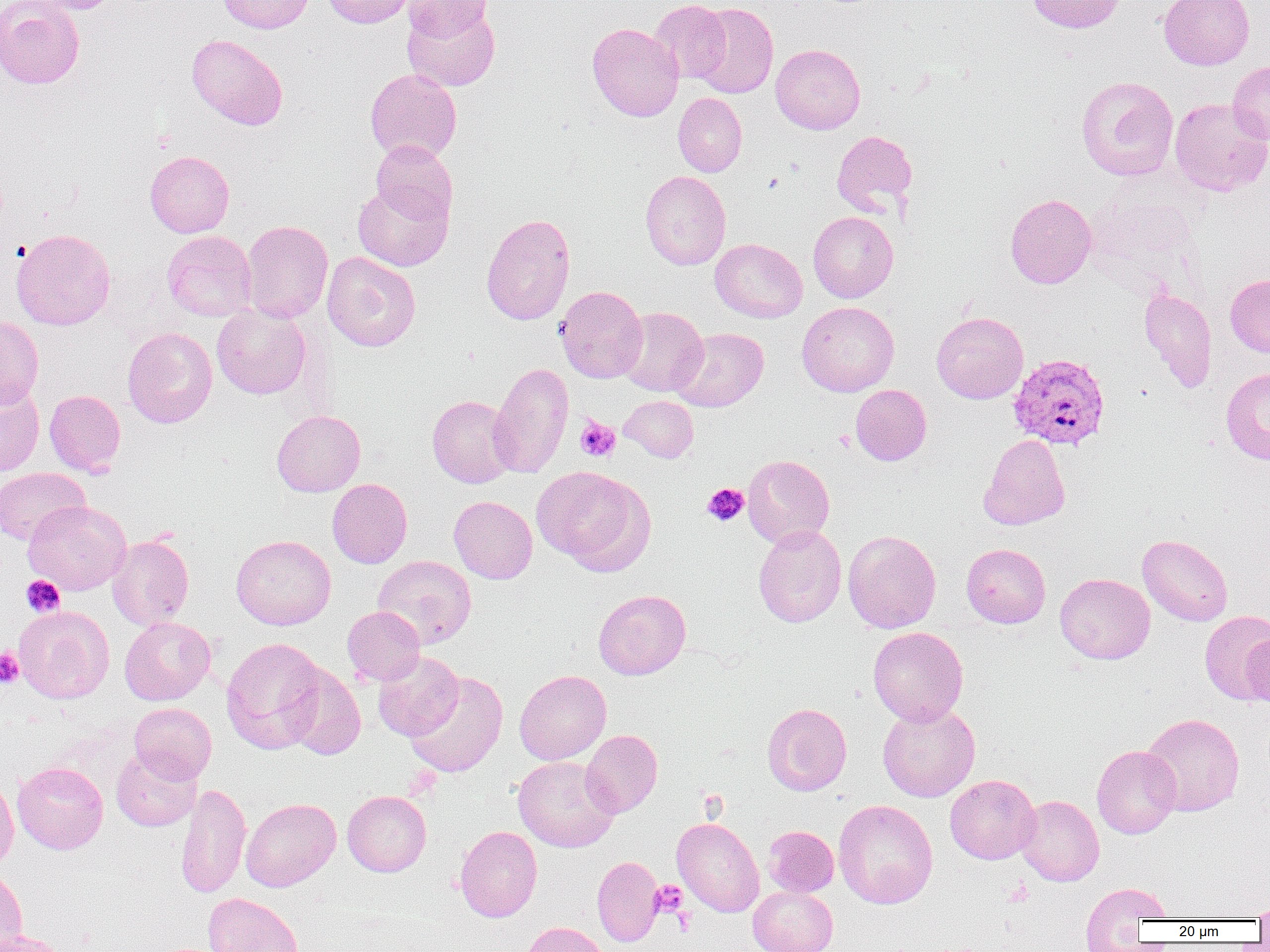
Summary:
  - Coordinate format: approximate bounding boxes as (x1,y1)-(x2,y2) corner pairs in pixels
  - Platelet locations: (576,416)-(621,462), (702,483)-(748,526), (21,575)-(65,617), (0,648)-(24,688), (1003,879)-(1032,907), (650,880)-(687,917)
  - Uninfected red blood cell locations: (0,0)-(85,89), (27,0)-(122,14), (216,0)-(314,33), (320,0)-(417,28), (403,0)-(492,41), (648,0)-(731,84), (1027,0)-(1126,33), (1159,0)-(1254,70), (693,2)-(779,98), (401,3)-(500,92), (587,23)-(683,122), (186,34)-(288,130), (771,44)-(866,134), (1227,61)-(1270,146), (365,68)-(462,163), (1076,75)-(1178,181), (673,92)-(747,177), (1170,98)-(1270,196), (831,130)-(917,217), (371,140)-(458,225), (145,150)-(234,238), (640,170)-(731,270), (353,180)-(453,271), (1084,190)-(1201,285), (1005,194)-(1096,288), (808,211)-(898,303), (481,213)-(576,325), (240,220)-(333,323), (11,228)-(115,330), (162,230)-(256,321), (710,238)-(807,322), (322,252)-(421,351), (1226,274)-(1270,357), (555,285)-(647,382), (1139,288)-(1216,393), (797,301)-(899,396), (212,304)-(311,400), (616,307)-(708,396), (931,311)-(1028,404), (0,315)-(44,408), (123,327)-(217,428), (670,327)-(769,412), (489,362)-(573,479), (1221,367)-(1270,465), (0,382)-(44,476), (850,385)-(931,465), (44,389)-(125,477), (427,395)-(517,488), (619,395)-(698,462), (272,410)-(365,496), (980,434)-(1070,530), (743,454)-(835,548), (532,466)-(654,574), (0,467)-(90,545), (327,478)-(412,568), (449,495)-(537,584), (23,501)-(131,595), (753,525)-(846,627), (843,529)-(941,633), (1137,534)-(1233,626), (107,535)-(194,629), (231,535)-(336,630), (961,543)-(1051,628), (373,555)-(476,649), (1055,573)-(1155,664), (593,589)-(691,680), (14,606)-(114,703), (342,606)-(425,686), (1199,610)-(1270,705), (119,616)-(216,705), (868,626)-(968,726), (1242,631)-(1270,707), (221,637)-(328,754), (372,650)-(464,741), (282,663)-(366,759), (514,670)-(611,765), (404,671)-(508,777), (129,703)-(216,783), (762,703)-(851,795), (877,703)-(980,801), (1140,713)-(1245,816), (581,730)-(663,817), (1092,745)-(1181,839), (112,748)-(201,831), (513,756)-(620,853), (12,762)-(108,854), (0,771)-(18,873), (945,774)-(1041,864), (176,783)-(251,899), (342,790)-(431,876), (1016,795)-(1104,886), (241,798)-(341,892), (834,799)-(938,909), (672,817)-(765,917), (454,825)-(542,922), (763,825)-(839,896), (592,856)-(664,946), (0,868)-(27,952), (1080,882)-(1173,947), (748,885)-(838,952), (203,892)-(303,952), (1252,897)-(1270,923), (519,921)-(610,952), (1,929)-(68,952)
  - Plasmodium vivax-infected red blood cell locations: (1007,344)-(1109,441)
  - Slide-level diagnosis: Plasmodium vivax
  - Field of view: single
  - Modality: optical microscopy
  - Preparation: thin blood smear
  - Image size: 1270×952 pixels
  - Magnification: 1000x